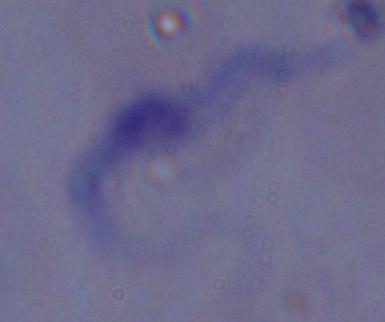

A trypanosome is seen. Micrograph. 1000x magnification.